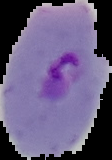
image size = 112×160 pixels
malaria status = parasitized
preparation = thin blood film
image type = cell region segmented out of the field of view; surrounding area masked to black